Identify the parasite.
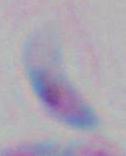

This is Toxoplasma gondii.

modality = micrograph
magnification = 1000x